Give the position of every Plasmodium parasite and every leukocyte.
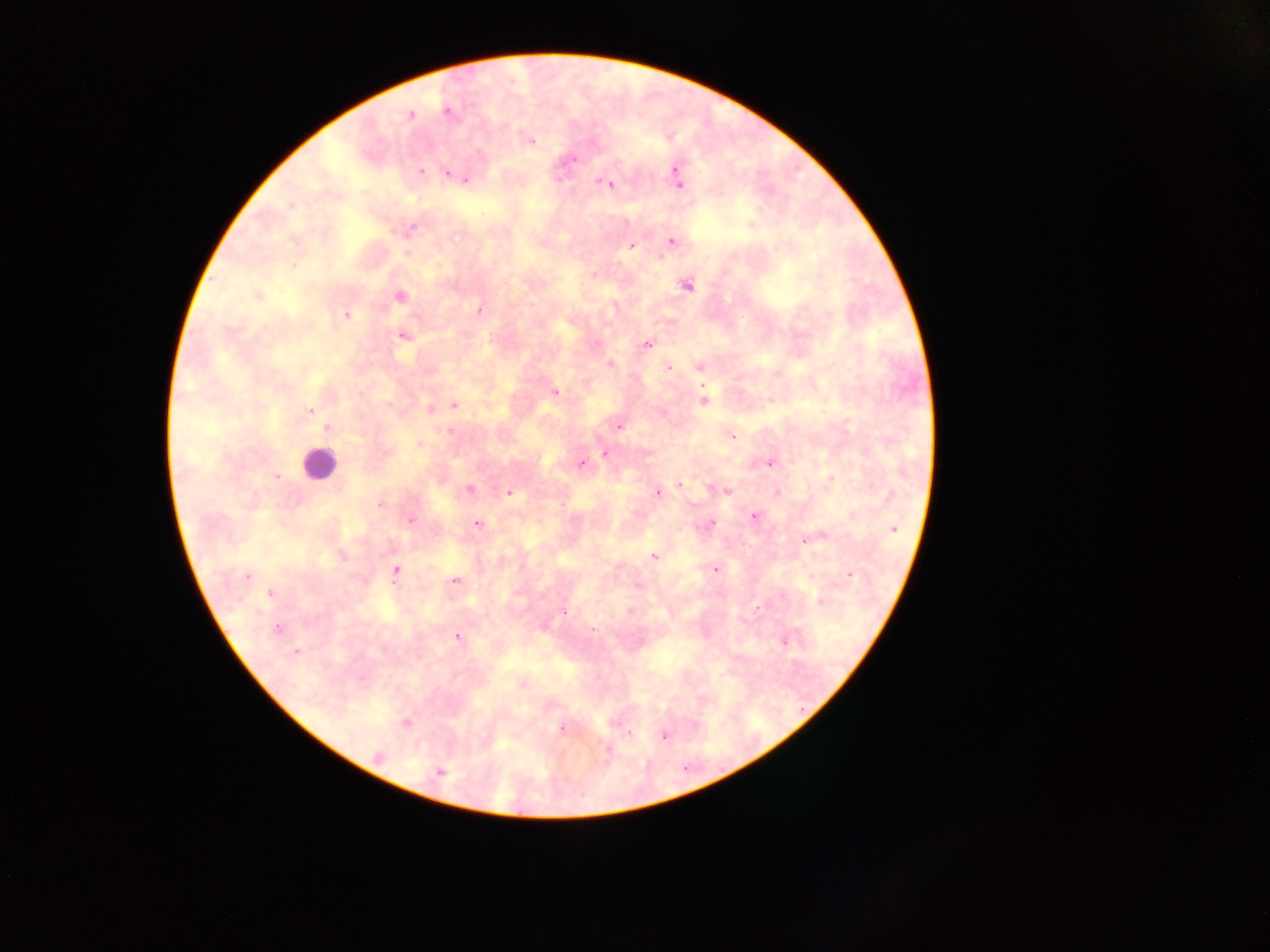

Approximate centers as [x, y] in pixels.
Plasmodium parasites: [448, 112], [410, 114], [530, 141], [573, 160], [421, 172], [448, 174], [677, 174], [465, 180], [610, 183], [679, 183], [290, 206], [412, 228], [671, 241], [632, 246], [408, 253], [687, 286], [257, 295], [400, 296], [479, 310], [346, 315], [402, 336], [647, 344], [610, 365], [668, 367], [699, 367], [555, 391], [704, 401], [455, 405], [429, 408], [310, 411], [618, 427], [329, 428], [732, 436], [605, 453], [581, 463], [770, 463], [277, 476], [831, 478], [681, 484], [469, 489], [727, 492], [509, 493], [656, 493], [380, 505], [754, 516], [410, 521], [711, 523], [477, 524], [894, 529], [807, 540], [654, 557], [715, 569], [395, 570], [850, 575], [246, 576], [455, 580], [270, 594], [820, 602], [564, 612], [277, 629], [457, 637], [784, 641], [296, 651], [406, 722], [562, 729], [629, 734], [664, 736], [608, 751], [379, 756], [440, 772].
Leukocytes: [319, 465].

field of view = single
country = Ghana
preparation = thick blood smear
capture = mobile-phone photograph through a microscope
image size = 1270×952 pixels